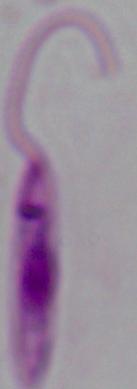
Summary:
  - Magnification: 1000x
  - Identification: Leishmania
  - Modality: photomicrograph